Assess this cell for malaria.
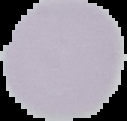
Uninfected.

image type = segmented cell region with the area outside set to black
image size = 127×121 pixels
preparation = thin blood smear